Classify this cell by malaria status.
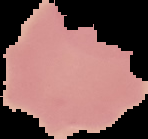

Uninfected.

Summary:
  - Preparation: thin blood film
  - Image size: 148×139 pixels
  - Image type: cell region segmented out of the field of view; surrounding area masked to black